Report the malaria status of this cell.
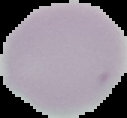

Uninfected.

image_size: 127×118 pixels
image_type: cell region segmented out of the field of view; surrounding area masked to black
preparation: thin blood film